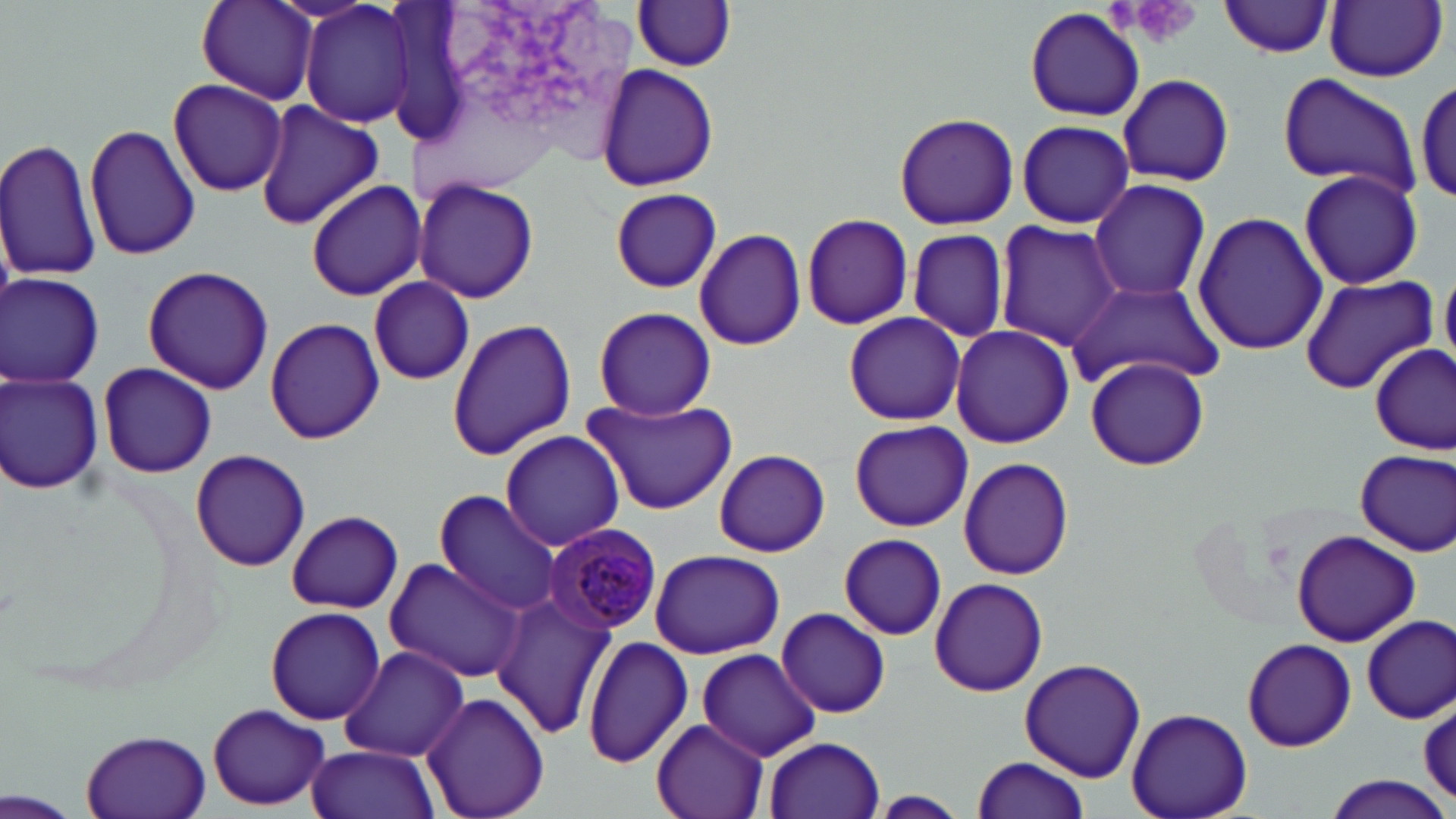
{
  "slide_level_diagnosis": "Plasmodium malariae",
  "uninfected_red_blood_cell_locations": "approximate bounding boxes as (x1, y1, x2, y2) in pixels: (195, 0, 318, 104), (299, 0, 415, 129), (1219, 1, 1336, 58), (1324, 1, 1447, 81), (633, 2, 738, 71), (1025, 7, 1144, 122), (594, 64, 719, 191), (1116, 72, 1235, 187), (1277, 73, 1421, 198), (1415, 75, 1456, 205), (166, 78, 287, 197), (254, 100, 384, 230), (892, 111, 1019, 231), (1013, 120, 1137, 229), (84, 121, 200, 261), (0, 137, 101, 284), (1297, 168, 1424, 289), (414, 176, 539, 303), (1089, 177, 1212, 302), (304, 178, 425, 302), (609, 188, 724, 292), (1192, 210, 1327, 358), (802, 215, 913, 330), (994, 221, 1125, 352), (694, 227, 807, 351), (906, 227, 1011, 343), (141, 265, 275, 395), (1439, 272, 1455, 365), (1, 273, 105, 387), (1299, 275, 1438, 394), (368, 277, 475, 386), (1066, 283, 1223, 390), (593, 306, 715, 421), (842, 310, 965, 425), (447, 315, 577, 461), (264, 317, 384, 446), (949, 323, 1074, 449), (1372, 345, 1454, 454), (1086, 356, 1210, 471), (97, 363, 217, 475), (1, 372, 104, 495), (582, 395, 739, 516), (849, 420, 973, 532), (498, 429, 625, 551), (713, 448, 830, 557), (188, 449, 311, 573), (1354, 450, 1455, 556), (956, 457, 1077, 579), (432, 495, 561, 614), (286, 510, 404, 613), (1290, 529, 1421, 647), (839, 534, 947, 640), (649, 548, 784, 659), (382, 557, 530, 684), (927, 577, 1049, 698), (491, 594, 618, 741), (264, 605, 387, 726), (775, 607, 891, 718), (1358, 614, 1454, 724), (584, 635, 694, 768), (1241, 637, 1356, 753), (337, 645, 471, 763), (696, 648, 821, 761), (1019, 658, 1144, 782), (418, 693, 550, 819), (1417, 696, 1456, 803), (207, 704, 331, 810), (1127, 707, 1252, 819), (651, 718, 772, 819), (76, 729, 213, 819), (763, 735, 885, 819), (306, 744, 439, 819), (969, 754, 1092, 818), (1320, 775, 1453, 819), (2, 788, 79, 819), (868, 791, 970, 817)",
  "modality": "light microscopy",
  "field_of_view": "one of a larger specimen",
  "stain": "May-Grünwald-Giemsa",
  "magnification": "1000x",
  "preparation": "thin blood smear",
  "image_size": "1456×819 pixels",
  "platelet_locations": "approximate bounding boxes as (x1, y1, x2, y2) in pixels: (1115, 0, 1204, 50)",
  "plasmodium_malariae_infected_red_blood_cell_locations": "approximate bounding boxes as (x1, y1, x2, y2) in pixels: (543, 522, 663, 636)"
}